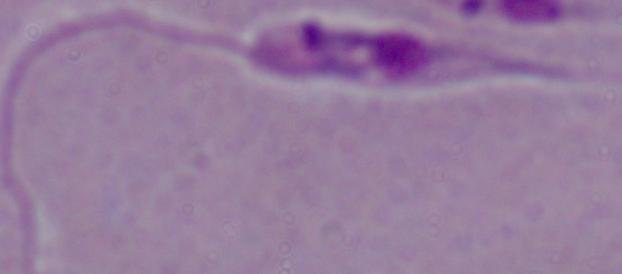

{
  "identification": "Leishmania",
  "magnification": "1000x",
  "modality": "micrograph"
}